Identify the blood parasite species.
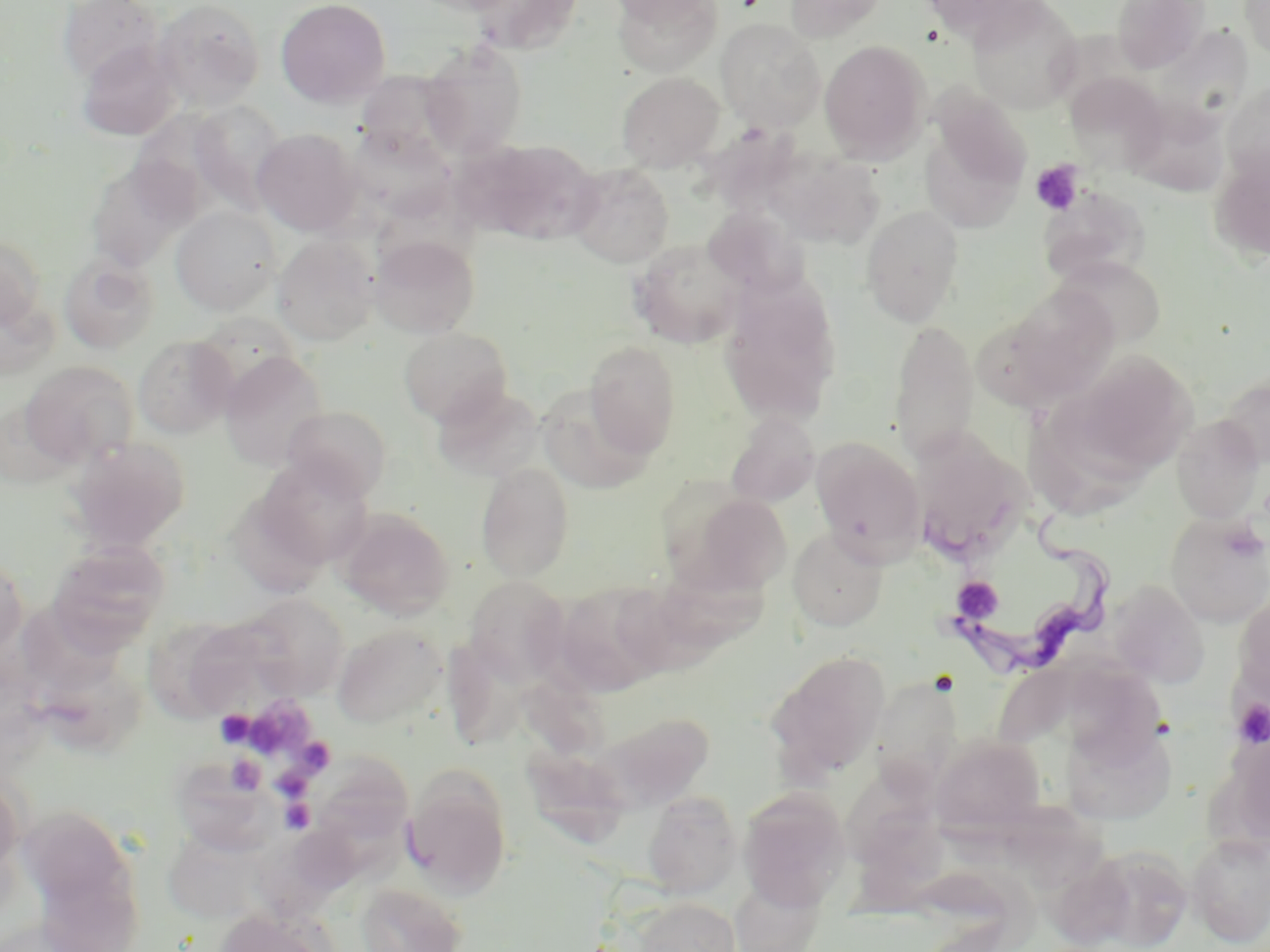

Trypanosoma brucei.

Approximate bounding boxes as [x1, y1, x2, y2] in pixels. Platelet locations: [1030, 160, 1084, 216], [952, 576, 1003, 624], [1232, 698, 1270, 747], [215, 710, 255, 747], [226, 755, 266, 794], [271, 769, 312, 801], [281, 798, 316, 832]. Trypanosoma brucei locations: [947, 508, 1122, 680]. Uninfected red blood cell locations: [58, 0, 163, 85], [152, 0, 265, 110], [275, 0, 391, 108], [467, 0, 585, 55], [606, 0, 715, 25], [612, 0, 722, 78], [785, 0, 889, 41], [918, 0, 1046, 39], [966, 0, 1083, 114], [1111, 0, 1209, 73], [1239, 0, 1270, 62], [716, 18, 825, 131], [1157, 29, 1263, 143], [76, 40, 182, 141], [819, 40, 931, 162], [419, 44, 527, 160], [358, 67, 478, 167], [616, 72, 724, 172], [1065, 72, 1169, 172], [1221, 80, 1270, 188], [924, 87, 1036, 217], [1127, 98, 1239, 197], [189, 100, 290, 212], [252, 129, 363, 236], [474, 140, 598, 244], [764, 147, 886, 250], [1208, 150, 1270, 264], [86, 160, 194, 272], [567, 163, 674, 268], [1040, 186, 1152, 280], [171, 206, 281, 315], [703, 206, 807, 298], [860, 206, 964, 326], [272, 234, 380, 345], [369, 234, 480, 338], [0, 235, 47, 328], [628, 238, 746, 348], [58, 253, 159, 354], [1054, 255, 1166, 349], [720, 278, 842, 425], [1001, 284, 1120, 401], [889, 320, 979, 464], [399, 326, 512, 426], [132, 335, 236, 438], [584, 341, 681, 455], [219, 351, 329, 472], [1063, 351, 1196, 478], [21, 361, 138, 467], [1219, 373, 1269, 467], [431, 384, 542, 481], [535, 384, 657, 495], [7, 385, 100, 487], [281, 405, 392, 501], [725, 413, 819, 507], [1171, 415, 1265, 523], [1024, 419, 1139, 521], [910, 434, 1032, 563], [66, 436, 190, 552], [811, 437, 925, 562], [253, 457, 374, 568], [476, 462, 575, 581], [682, 493, 792, 594], [339, 510, 455, 619], [1165, 512, 1270, 627], [788, 528, 888, 631], [46, 541, 170, 649], [0, 549, 27, 660], [664, 551, 782, 656], [463, 576, 569, 680], [1108, 580, 1208, 687], [553, 581, 668, 695], [1232, 589, 1270, 709], [241, 593, 349, 699], [164, 615, 280, 720], [333, 624, 447, 728], [441, 632, 544, 754], [31, 646, 146, 757], [766, 650, 890, 784], [518, 660, 617, 762], [1062, 662, 1173, 743], [870, 680, 958, 808], [596, 711, 718, 809], [1062, 717, 1178, 826], [930, 735, 1046, 837], [521, 741, 629, 854], [310, 755, 414, 848], [182, 760, 285, 855], [404, 769, 512, 899], [0, 774, 25, 890], [736, 786, 851, 910], [642, 790, 742, 897], [1014, 803, 1111, 894], [17, 804, 134, 904], [856, 815, 950, 918], [169, 832, 271, 923], [1187, 833, 1270, 946], [1079, 845, 1193, 951], [730, 874, 827, 952], [355, 881, 467, 952], [633, 896, 741, 952], [211, 908, 335, 952]. Optical microscopy. Image is 1270×952 pixels. Captured at 1000x magnification. Single field of view. May-Grünwald-Giemsa stain. Thin blood film.